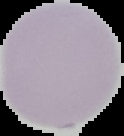
Summary:
  - Preparation: thin blood smear
  - Image type: segmented cell region with the area outside set to black
  - Result: no Plasmodium parasites seen
  - Image size: 124×136 pixels